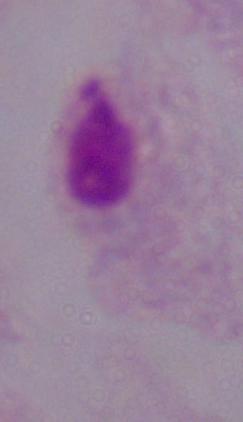

modality = photomicrograph
magnification = 1000x
identification = trichomonad